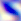
Micrograph. Captured at 400x magnification. Toxoplasma gondii is seen.